Name the parasite shown.
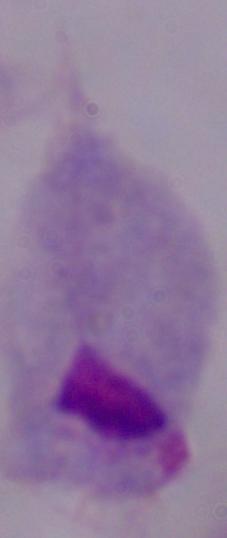

A trichomonad.

Summary:
  - Magnification: 1000x
  - Modality: photomicrograph